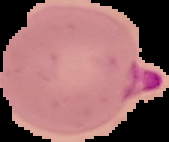

result: Plasmodium parasites detected
preparation: thin blood smear
image_type: segmented cell region with the area outside set to black
image_size: 169×142 pixels